Outline each white blood cell.
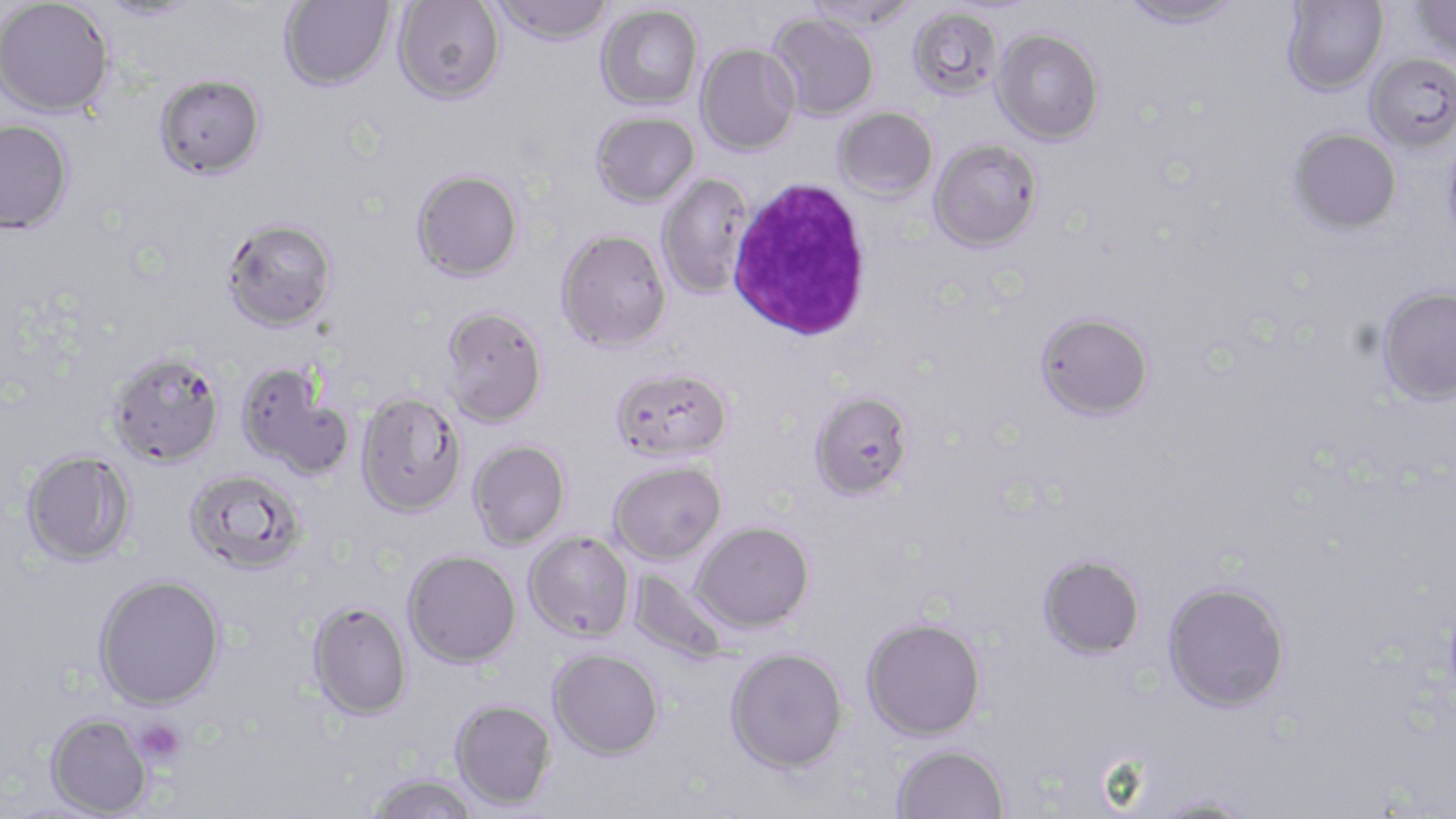

Approximate bounding boxes as named x1/y1/x2/y2 corners in pixels.
White blood cells: (x1=726, y1=177, x2=874, y2=341).

Summary:
  - Uninfected red blood cell locations: (x1=278, y1=0, x2=395, y2=90), (x1=491, y1=0, x2=613, y2=44), (x1=803, y1=0, x2=921, y2=31), (x1=1118, y1=0, x2=1243, y2=29), (x1=1281, y1=0, x2=1388, y2=96), (x1=1412, y1=0, x2=1456, y2=62), (x1=0, y1=1, x2=114, y2=117), (x1=96, y1=1, x2=205, y2=22), (x1=394, y1=1, x2=505, y2=103), (x1=596, y1=4, x2=703, y2=110), (x1=907, y1=6, x2=1004, y2=101), (x1=768, y1=13, x2=879, y2=121), (x1=991, y1=29, x2=1104, y2=145), (x1=696, y1=43, x2=800, y2=155), (x1=1365, y1=53, x2=1456, y2=154), (x1=155, y1=73, x2=266, y2=179), (x1=833, y1=107, x2=938, y2=202), (x1=591, y1=111, x2=699, y2=208), (x1=0, y1=118, x2=74, y2=233), (x1=1289, y1=127, x2=1401, y2=233), (x1=1442, y1=131, x2=1456, y2=255), (x1=928, y1=139, x2=1043, y2=252), (x1=411, y1=169, x2=523, y2=281), (x1=658, y1=173, x2=754, y2=300), (x1=221, y1=218, x2=337, y2=331), (x1=556, y1=229, x2=671, y2=351), (x1=1375, y1=286, x2=1456, y2=407), (x1=439, y1=305, x2=548, y2=427), (x1=1035, y1=313, x2=1154, y2=420), (x1=108, y1=351, x2=225, y2=468), (x1=235, y1=361, x2=355, y2=480), (x1=611, y1=367, x2=732, y2=463), (x1=809, y1=390, x2=913, y2=500), (x1=356, y1=392, x2=467, y2=517), (x1=468, y1=440, x2=570, y2=549), (x1=21, y1=450, x2=137, y2=567), (x1=609, y1=461, x2=727, y2=565), (x1=184, y1=469, x2=307, y2=574), (x1=691, y1=521, x2=814, y2=633), (x1=523, y1=531, x2=635, y2=641), (x1=403, y1=549, x2=521, y2=668), (x1=1038, y1=554, x2=1145, y2=659), (x1=629, y1=570, x2=729, y2=663), (x1=92, y1=573, x2=227, y2=710), (x1=1162, y1=581, x2=1290, y2=713), (x1=307, y1=600, x2=412, y2=720), (x1=861, y1=615, x2=987, y2=740), (x1=726, y1=647, x2=848, y2=773), (x1=548, y1=648, x2=664, y2=761), (x1=451, y1=699, x2=557, y2=810), (x1=46, y1=712, x2=153, y2=817), (x1=891, y1=743, x2=1010, y2=819), (x1=367, y1=772, x2=479, y2=818), (x1=1146, y1=796, x2=1261, y2=818)
  - Platelet locations: (x1=133, y1=719, x2=187, y2=767)
  - Slide-level diagnosis: Plasmodium falciparum
  - Image size: 1456×819 pixels
  - Preparation: thin blood smear
  - Magnification: 1000x
  - Modality: optical microscopy
  - Stain: May-Grünwald-Giemsa
  - Field of view: one of a larger specimen